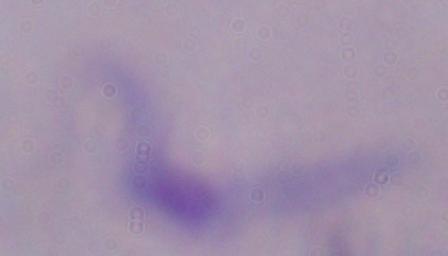

Summary:
  - Modality: micrograph
  - Identification: trypanosome
  - Magnification: 1000x